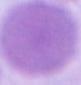

modality = photomicrograph
magnification = 1000x
identification = erythrocyte